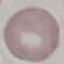

malaria status = uninfected
image type = cell patch, automatically extracted from a larger field of view and resized to 64 × 64 pixels
stain = Giemsa
capture = smartphone camera at the microscope eyepiece
preparation = thin blood smear